Report the malaria status of this cell.
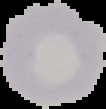
It is uninfected.

Summary:
  - Preparation: thin blood film
  - Image type: segmented cell region on a black background
  - Image size: 106×109 pixels